Assess this cell for malaria.
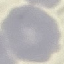

Uninfected.

stain = Giemsa
image type = automatically extracted cell patch, resized to 64 × 64 pixels
capture = smartphone camera at the microscope eyepiece
preparation = thin smear